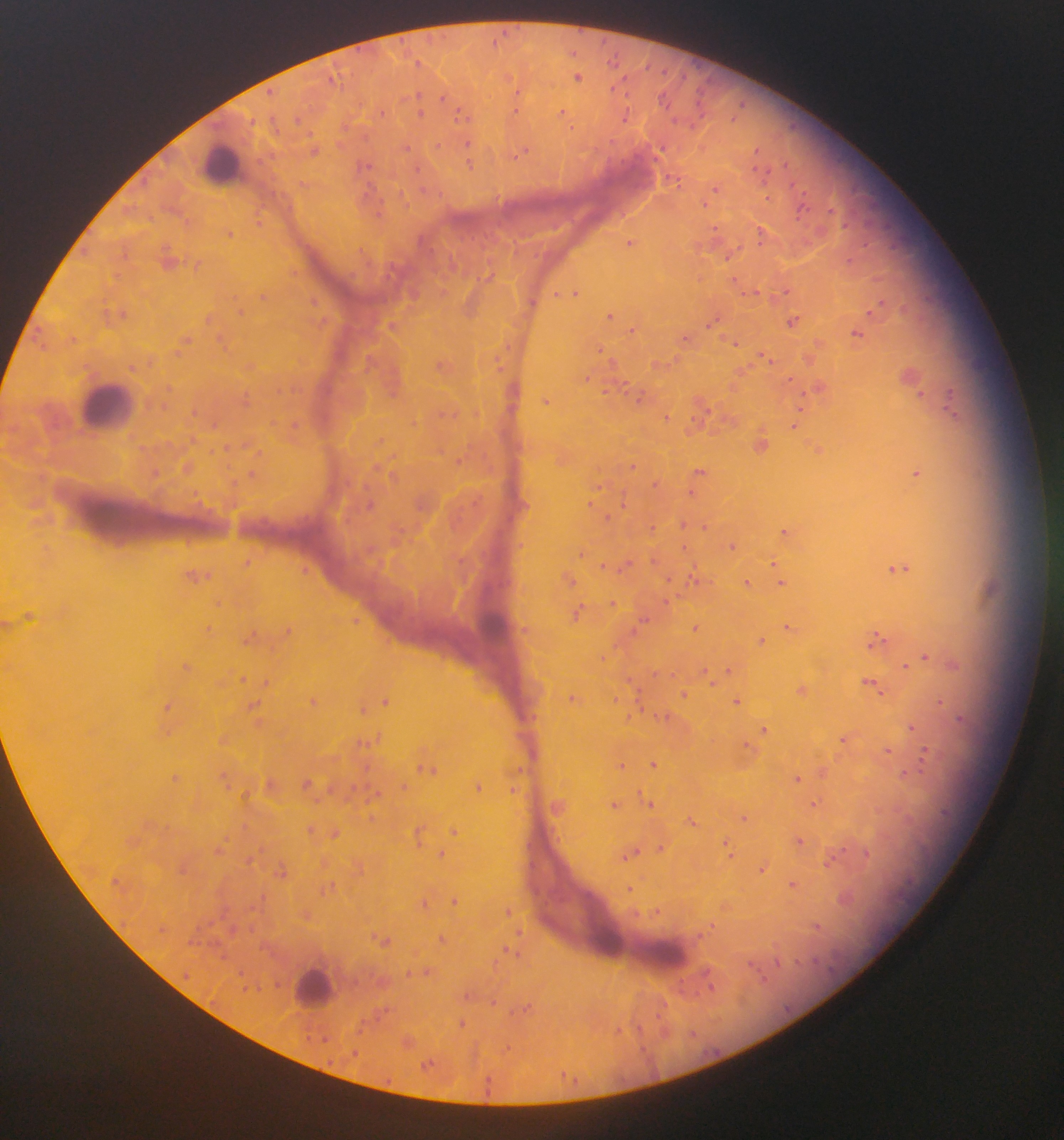 Approximate centers as {x, y} in pixels. Leukocyte locations: {101, 402}, {495, 621}, {606, 932}, {663, 949}, {310, 981}. Malaria parasite locations: {493, 40}, {602, 40}, {360, 52}, {574, 54}, {615, 58}, {418, 61}, {648, 67}, {577, 76}, {626, 76}, {683, 78}, {709, 80}, {335, 84}, {271, 91}, {518, 92}, {626, 94}, {421, 95}, {662, 100}, {699, 104}, {742, 105}, {456, 109}, {514, 110}, {565, 112}, {382, 115}, {420, 117}, {623, 121}, {253, 122}, {299, 122}, {276, 124}, {573, 130}, {309, 133}, {439, 143}, {470, 143}, {406, 146}, {313, 149}, {759, 150}, {518, 156}, {260, 160}, {787, 163}, {470, 164}, {754, 166}, {371, 168}, {419, 170}, {675, 181}, {302, 182}, {146, 185}, {717, 189}, {423, 190}, {402, 193}, {442, 195}, {801, 205}, {831, 208}, {187, 222}, {258, 223}, {716, 226}, {231, 234}, {759, 236}, {629, 242}, {126, 257}, {727, 259}, {196, 266}, {295, 273}, {117, 275}, {784, 291}, {556, 293}, {577, 293}, {744, 293}, {264, 297}, {234, 298}, {106, 300}, {315, 300}, {534, 302}, {610, 313}, {125, 314}, {245, 314}, {208, 317}, {109, 319}, {797, 320}, {323, 321}, {708, 323}, {633, 329}, {222, 337}, {685, 338}, {189, 341}, {738, 342}, {509, 347}, {602, 349}, {226, 351}, {179, 354}, {768, 357}, {151, 363}, {370, 370}, {620, 383}, {299, 389}, {951, 389}, {171, 390}, {278, 392}, {604, 392}, {920, 392}, {249, 394}, {640, 395}, {803, 400}, {163, 405}, {245, 405}, {708, 409}, {194, 411}, {441, 413}, {667, 416}, {952, 416}, {691, 419}, {414, 423}, {276, 425}, {294, 425}, {794, 426}, {194, 440}, {381, 441}, {170, 444}, {227, 447}, {246, 447}, {146, 448}, {212, 451}, {260, 452}, {460, 461}, {634, 465}, {188, 467}, {230, 467}, {377, 467}, {701, 468}, {156, 473}, {253, 473}, {918, 473}, {393, 476}, {235, 483}, {653, 484}, {368, 487}, {601, 487}, {690, 491}, {196, 492}, {480, 496}, {475, 501}, {589, 504}, {234, 505}, {419, 506}, {461, 506}, {627, 507}, {610, 516}, {458, 519}, {263, 520}, {685, 524}, {652, 526}, {706, 527}, {401, 529}, {782, 530}, {189, 540}, {686, 546}, {730, 546}, {583, 553}, {656, 559}, {249, 564}, {603, 564}, {772, 564}, {621, 568}, {896, 569}, {305, 571}, {691, 575}, {198, 577}, {569, 577}, {668, 577}, {748, 582}, {779, 582}, {678, 595}, {614, 601}, {667, 602}, {219, 603}, {582, 606}, {644, 620}, {357, 624}, {695, 626}, {788, 628}, {289, 631}, {634, 632}, {251, 636}, {883, 637}, {762, 641}, {871, 645}, {616, 646}, {601, 657}, {927, 657}, {187, 666}, {906, 666}, {728, 671}, {656, 674}, {670, 676}, {707, 676}, {246, 677}, {629, 678}, {871, 680}, {265, 683}, {881, 694}, {685, 695}, {737, 697}, {570, 699}, {615, 699}, {943, 700}, {315, 702}, {386, 702}, {256, 703}, {640, 705}, {169, 706}, {363, 710}, {667, 715}, {962, 720}, {910, 726}, {764, 728}, {843, 738}, {370, 743}, {891, 753}, {927, 761}, {623, 764}, {653, 764}, {368, 768}, {520, 768}, {435, 769}, {905, 773}, {797, 778}, {226, 779}, {176, 781}, {308, 783}, {402, 785}, {330, 787}, {353, 787}, {377, 787}, {478, 788}, {517, 791}, {246, 796}, {317, 801}, {371, 803}, {617, 804}, {652, 804}, {816, 804}, {747, 817}, {692, 820}, {311, 828}, {554, 828}, {456, 831}, {334, 833}, {727, 841}, {225, 842}, {561, 842}, {796, 843}, {663, 844}, {260, 848}, {844, 850}, {637, 851}, {440, 852}, {867, 854}, {731, 855}, {625, 860}, {830, 864}, {282, 867}, {361, 869}, {761, 869}, {790, 877}, {330, 886}, {634, 889}, {258, 900}, {455, 902}, {425, 903}, {508, 909}, {658, 911}, {638, 912}, {820, 925}, {712, 926}, {253, 928}, {521, 935}, {382, 937}, {442, 939}, {206, 941}, {507, 947}, {519, 956}, {819, 961}, {494, 962}, {777, 962}, {426, 970}, {241, 971}, {409, 971}, {760, 973}, {186, 978}, {683, 985}, {711, 986}, {466, 996}, {493, 1002}, {667, 1003}, {529, 1006}, {511, 1012}, {386, 1013}, {658, 1018}, {462, 1022}, {361, 1026}, {640, 1027}, {621, 1029}, {694, 1033}, {319, 1041}, {643, 1050}, {355, 1054}, {329, 1063}, {426, 1063}, {568, 1079}, {491, 1086}. Photographed through a microscope with a mobile-phone camera. Image is 1064×1140 pixels. One field of view. Thick blood smear. Collected in Ghana.